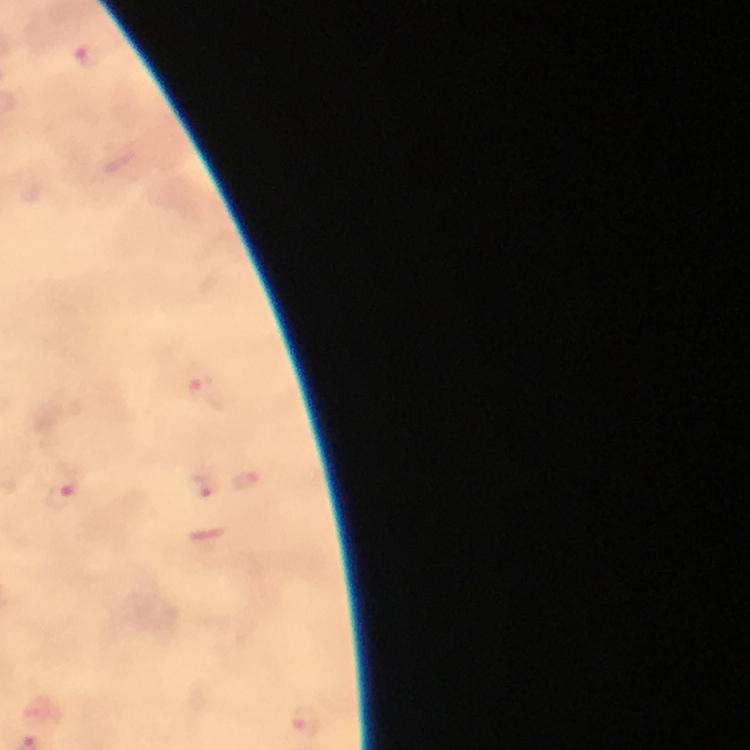

Approximate centers as (x, y) in pixels.
Summary:
  - Malaria parasite locations: (88, 55), (206, 393), (247, 481), (201, 487), (60, 494), (307, 720)
  - Image size: 750×750 pixels
  - Stain: Giemsa
  - Magnification: 100x
  - Preparation: thick blood smear
  - Context: from a malaria diagnostic workup
  - Immersion oil: applied
  - Capture: smartphone camera through the microscope
  - Cropped from: a single field of view